State which parasite is depicted.
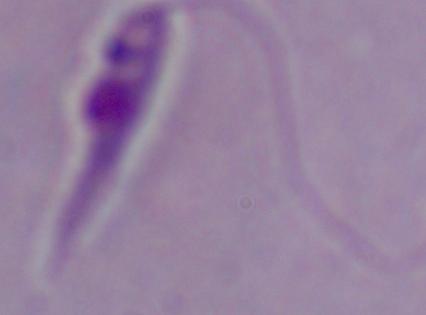

This is Leishmania.

{
  "magnification": "1000x",
  "modality": "micrograph"
}